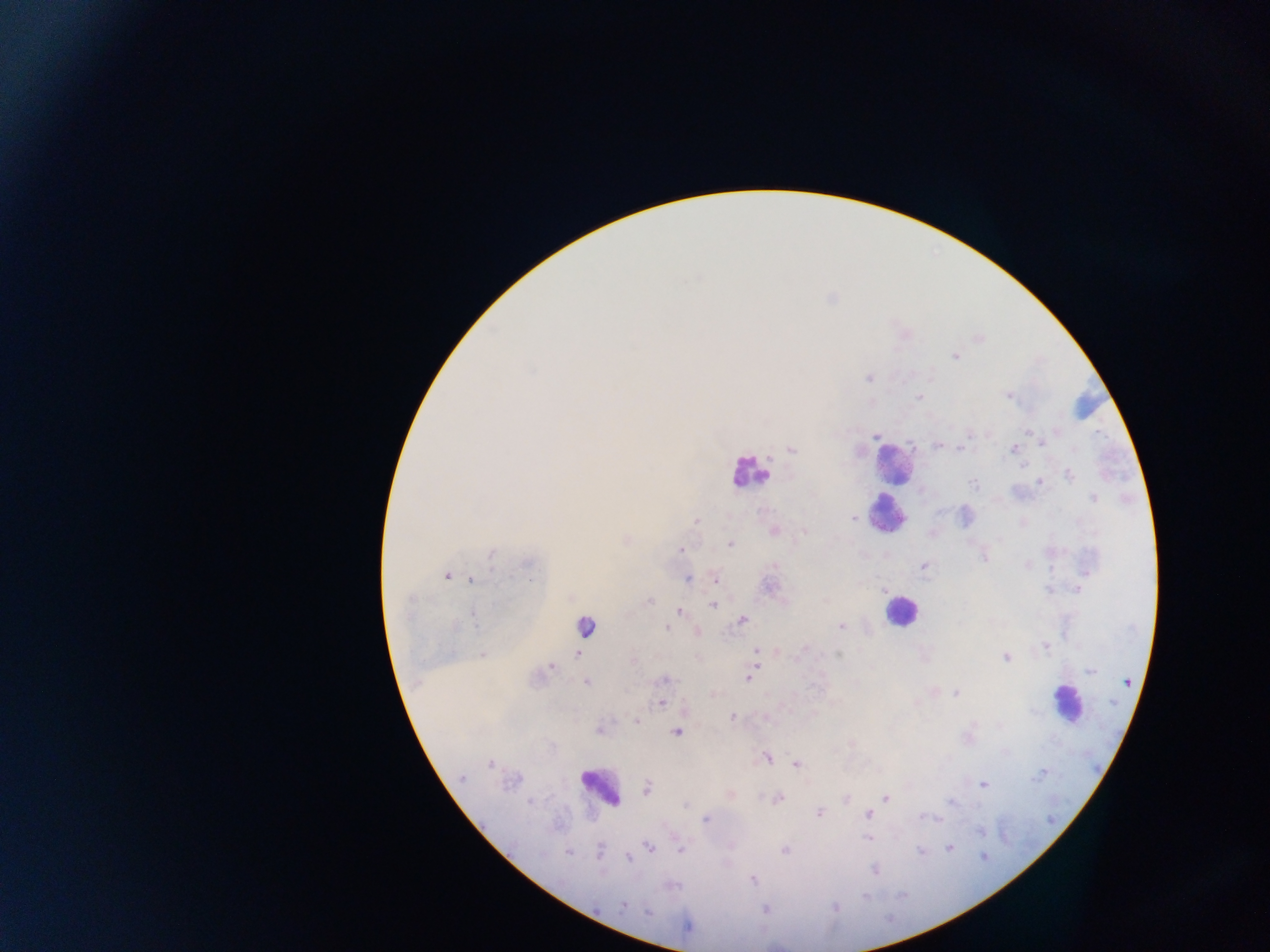

Approximate centers as (x, y) in pixels. Leukocyte locations: (1084, 402), (893, 464), (748, 472), (888, 514), (901, 611), (586, 625), (1066, 703), (600, 786). Malaria parasite locations: (955, 357), (868, 378), (1008, 397), (919, 398), (1028, 431), (972, 434), (877, 436), (1042, 442), (937, 445), (961, 447), (1013, 448), (791, 450), (1022, 466), (1069, 475), (1039, 482), (973, 484), (1093, 499), (853, 518), (695, 520), (774, 531), (804, 531), (730, 543), (681, 549), (491, 553), (985, 558), (528, 563), (1028, 564), (775, 565), (923, 566), (447, 575), (471, 579), (688, 579), (715, 579), (1078, 589), (1048, 590), (884, 591), (648, 601), (408, 602), (713, 605), (680, 612), (473, 614), (742, 620), (841, 626), (668, 628), (1045, 646), (805, 648), (757, 651), (577, 653), (482, 654), (838, 654), (1005, 657), (633, 661), (551, 667), (1090, 670), (749, 677), (663, 679), (1127, 681), (587, 683), (955, 693), (661, 703), (732, 717), (637, 721), (599, 730), (676, 732), (767, 757), (797, 763), (490, 764), (1039, 775), (461, 778), (983, 784), (648, 788), (886, 798), (778, 799), (845, 799), (530, 802), (951, 802), (686, 806), (819, 813), (868, 814), (922, 817), (706, 819), (980, 831), (868, 838), (649, 848), (950, 848), (680, 849), (784, 850), (600, 851), (921, 851), (568, 852), (629, 857), (983, 857), (875, 870), (752, 879), (865, 896), (623, 906), (835, 906), (765, 909), (648, 912), (686, 926). Sample from Ghana. Single field of view. Image is 1270×952 pixels. Mobile-phone photograph taken through the microscope. Thick blood smear.